Comment on the morphology of the erythrocytes.
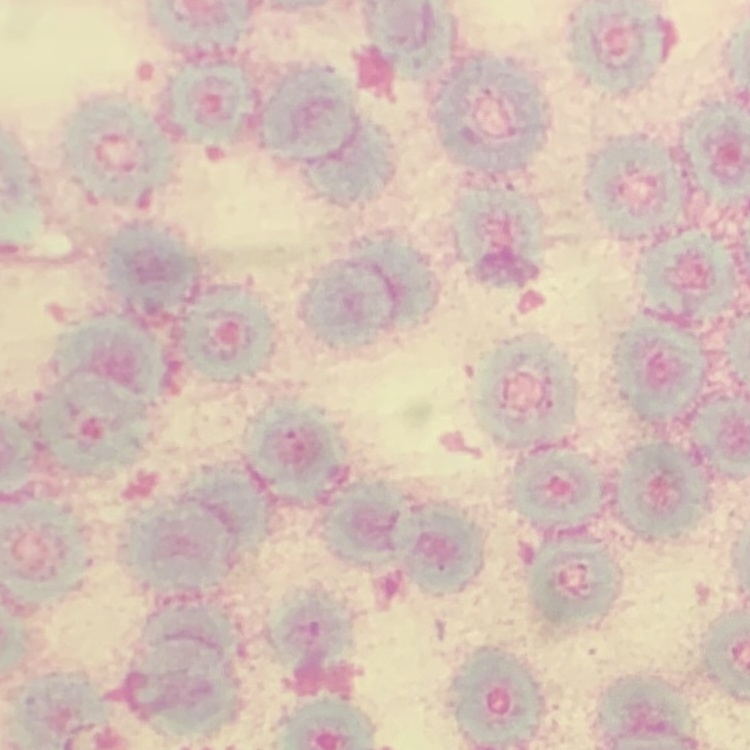

Rouleaux formation.

Summary:
  - Stain: Field's or Giemsa
  - Image type: one tile cut from a larger photomicrograph
  - Preparation: thin peripheral smear